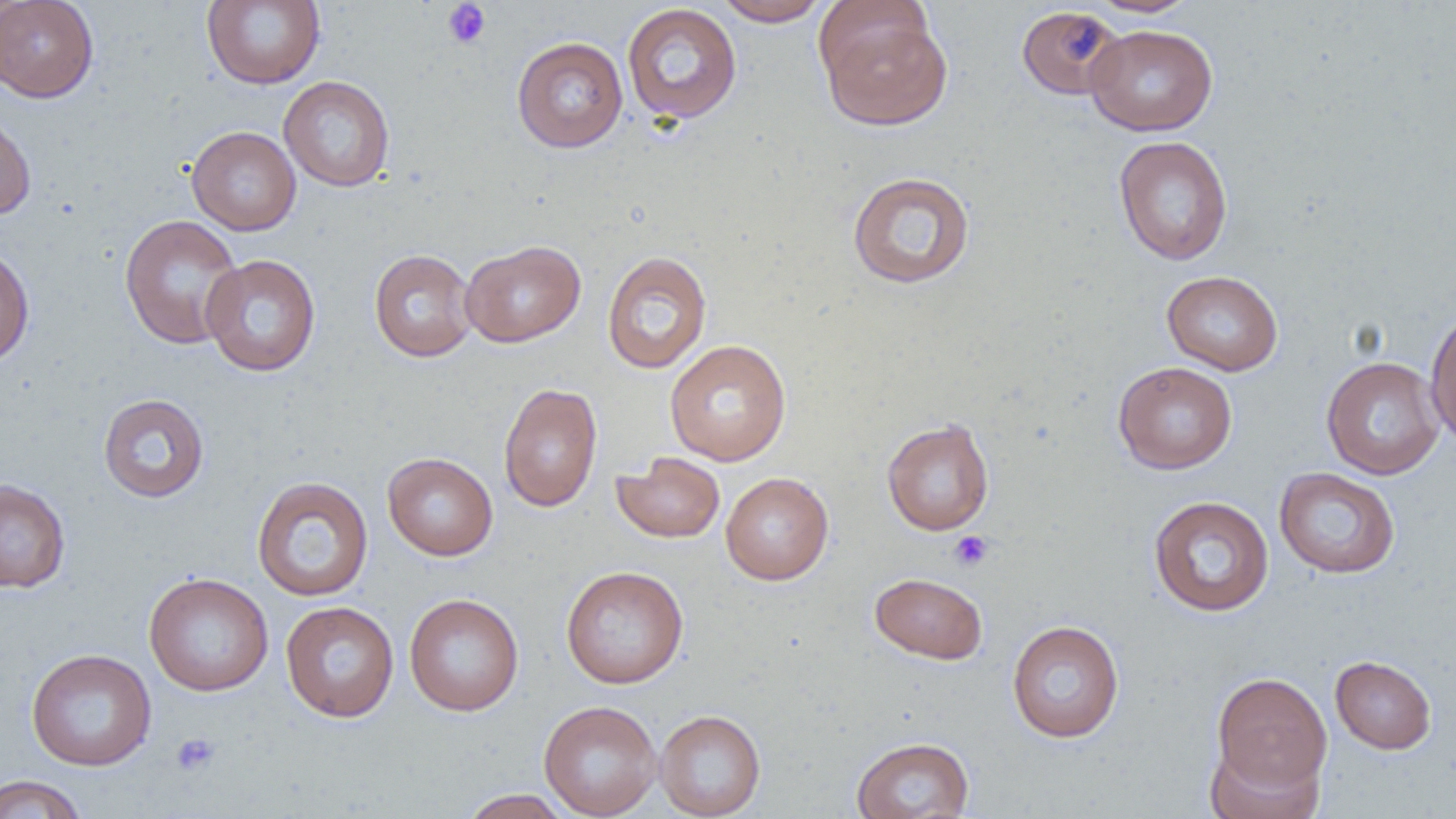

Approximate bounding boxes as named x1/y1/x2/y2 corners in pixels. Platelet locations: (x1=442, y1=1, x2=491, y2=50), (x1=949, y1=530, x2=994, y2=572), (x1=170, y1=732, x2=220, y2=777). Uninfected red blood cell locations: (x1=0, y1=0, x2=99, y2=102), (x1=201, y1=0, x2=326, y2=89), (x1=713, y1=0, x2=831, y2=26), (x1=1087, y1=0, x2=1202, y2=17), (x1=621, y1=3, x2=742, y2=125), (x1=1016, y1=5, x2=1125, y2=100), (x1=817, y1=7, x2=952, y2=130), (x1=1085, y1=23, x2=1218, y2=136), (x1=512, y1=36, x2=628, y2=153), (x1=279, y1=76, x2=395, y2=192), (x1=0, y1=105, x2=36, y2=219), (x1=186, y1=126, x2=302, y2=235), (x1=1113, y1=135, x2=1233, y2=266), (x1=846, y1=170, x2=976, y2=289), (x1=119, y1=214, x2=245, y2=350), (x1=460, y1=240, x2=586, y2=347), (x1=0, y1=242, x2=35, y2=367), (x1=368, y1=248, x2=478, y2=362), (x1=602, y1=250, x2=712, y2=374), (x1=201, y1=254, x2=321, y2=377), (x1=1161, y1=270, x2=1284, y2=376), (x1=1424, y1=305, x2=1456, y2=448), (x1=665, y1=339, x2=792, y2=466), (x1=1321, y1=356, x2=1445, y2=480), (x1=1112, y1=361, x2=1238, y2=475), (x1=498, y1=383, x2=603, y2=512), (x1=98, y1=393, x2=209, y2=503), (x1=881, y1=418, x2=995, y2=535), (x1=382, y1=452, x2=498, y2=561), (x1=611, y1=452, x2=725, y2=544), (x1=1274, y1=467, x2=1401, y2=579), (x1=720, y1=472, x2=834, y2=585), (x1=251, y1=475, x2=374, y2=602), (x1=0, y1=478, x2=71, y2=593), (x1=1148, y1=495, x2=1274, y2=616), (x1=560, y1=565, x2=689, y2=689), (x1=143, y1=572, x2=274, y2=696), (x1=869, y1=572, x2=988, y2=665), (x1=404, y1=593, x2=524, y2=716), (x1=280, y1=601, x2=400, y2=722), (x1=1006, y1=619, x2=1125, y2=743), (x1=26, y1=648, x2=157, y2=771), (x1=1330, y1=655, x2=1437, y2=754), (x1=1211, y1=671, x2=1332, y2=796), (x1=538, y1=700, x2=662, y2=818), (x1=654, y1=709, x2=766, y2=818), (x1=851, y1=736, x2=974, y2=819), (x1=1203, y1=738, x2=1325, y2=818), (x1=0, y1=774, x2=90, y2=819), (x1=459, y1=788, x2=573, y2=818). Slide-level diagnosis: no evidence of blood parasites. Image is 1456×819 pixels. Light microscopy. Thin blood smear. Single field of view. 1000x magnification.